State which cell type is depicted.
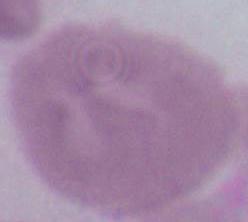
This is an erythrocyte.

Summary:
  - Magnification: 1000x
  - Modality: micrograph